Identify the parasite.
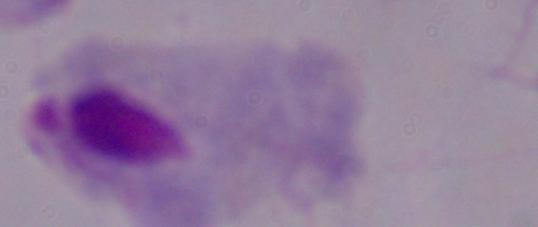
This is a trichomonad.

Summary:
  - Magnification: 1000x
  - Modality: micrograph